Report the malaria status of this cell.
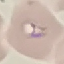
It is parasitized.

Thin blood smear. Giemsa stain. Acquired by smartphone through the microscope eyepiece. Automatically extracted cell patch, resized to 64 × 64 pixels.